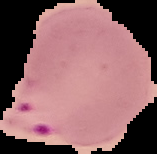

Summary:
  - Preparation: thin blood film
  - Image size: 157×154 pixels
  - Image type: segmented cell region with the area outside set to black
  - Result: malaria parasites detected